Locate every Plasmodium parasite.
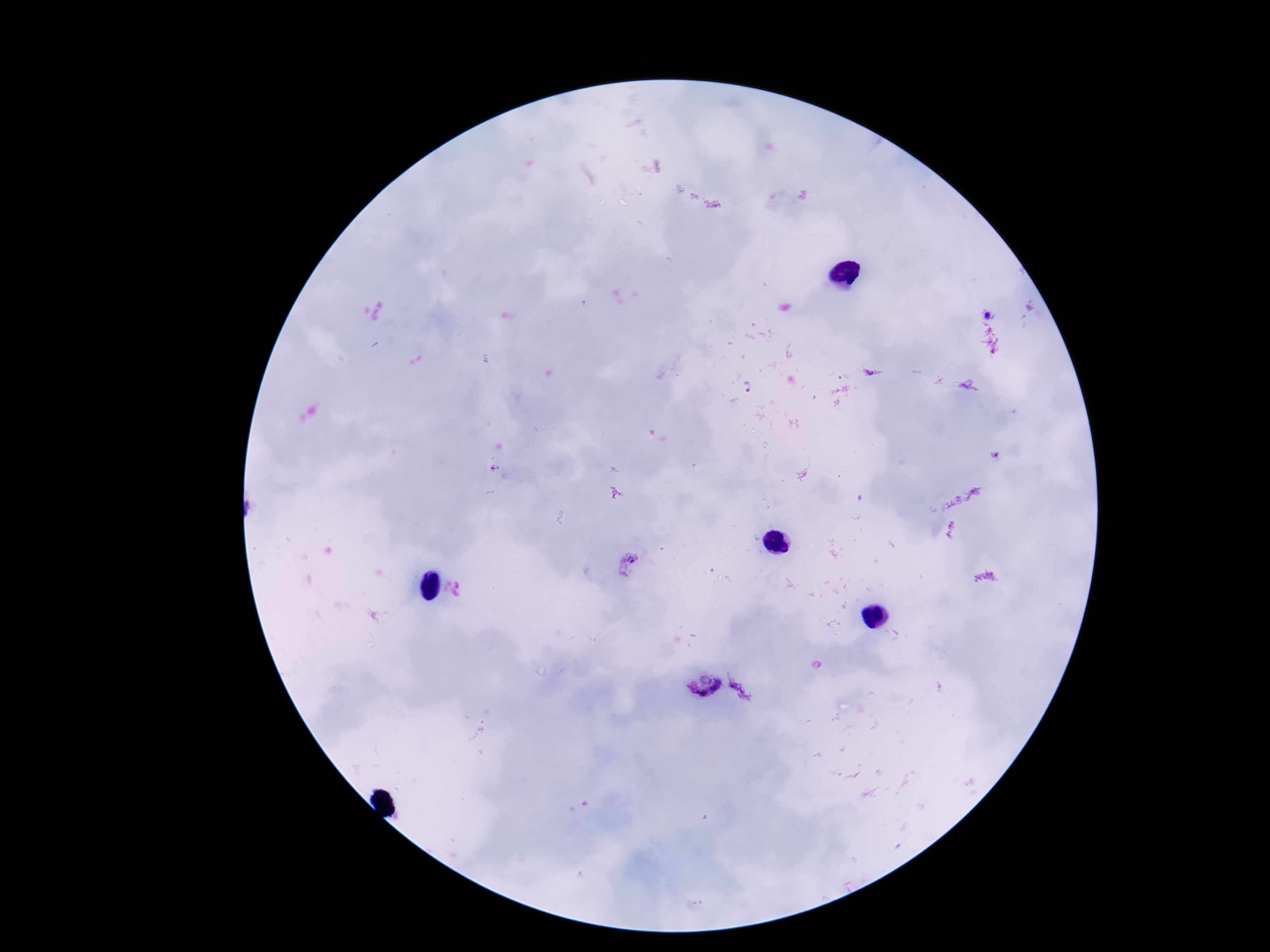
Approximate centers as [x, y] in pixels.
Plasmodium parasites: [629, 564], [703, 685].

Summary:
  - Stain: Giemsa
  - Capture: smartphone camera through the microscope eyepiece
  - Field of view: single
  - Patient malaria status: positive
  - Preparation: thick peripheral-blood smear
  - Magnification: 100x
  - Image size: 1270×952 pixels